Point out malaria parasites and leukocytes.
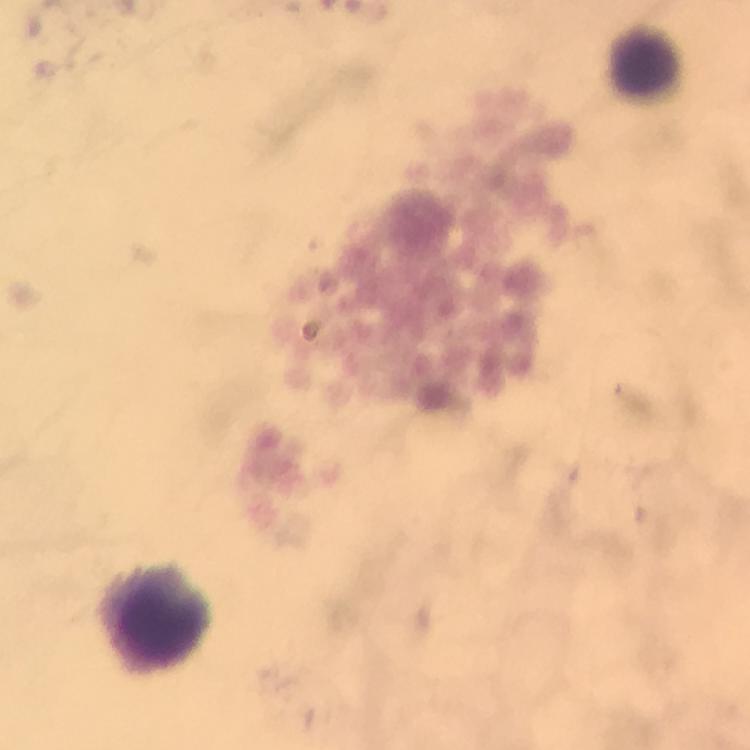
No malaria parasites detected.
Approximate centers as {x, y} in pixels.
Leukocytes: {642, 50}, {163, 613}.

Summary:
  - Stain: Giemsa
  - Immersion oil: applied
  - Image size: 750×750 pixels
  - Preparation: thick blood smear
  - Context: from a malaria diagnostic workup
  - Magnification: 100x
  - Cropped from: one field of view
  - Capture: smartphone mounted on the microscope